Assess this cell for malaria.
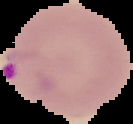
It is parasitized.

preparation = thin blood smear
image type = segmented cell region with the area outside set to black
image size = 133×124 pixels